Locate every leukocyte (white blood cell).
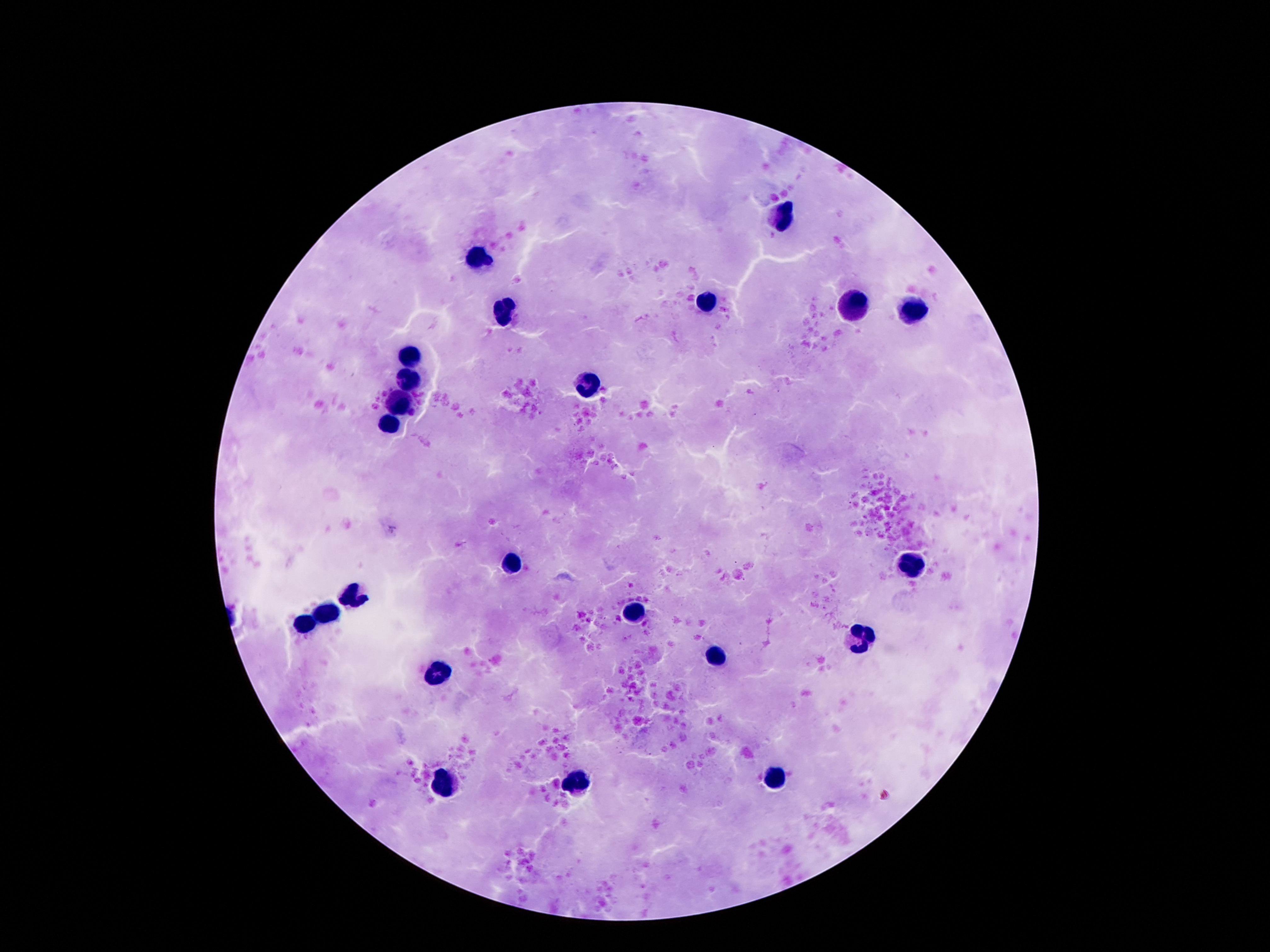
Approximate centers as {x, y} in pixels.
Leukocytes: {784, 215}, {478, 259}, {709, 302}, {853, 308}, {916, 311}, {506, 313}, {410, 357}, {408, 381}, {590, 385}, {403, 405}, {389, 423}, {513, 565}, {910, 565}, {352, 600}, {326, 614}, {634, 614}, {303, 623}, {865, 638}, {716, 657}, {438, 672}, {576, 780}, {774, 780}, {443, 784}.

Summary:
  - Stain: Giemsa
  - Preparation: thick peripheral-blood smear
  - Field of view: one from this slide
  - Magnification: 100x
  - Image size: 1270×952 pixels
  - Capture: smartphone camera through the microscope eyepiece
  - Patient malaria status: not infected